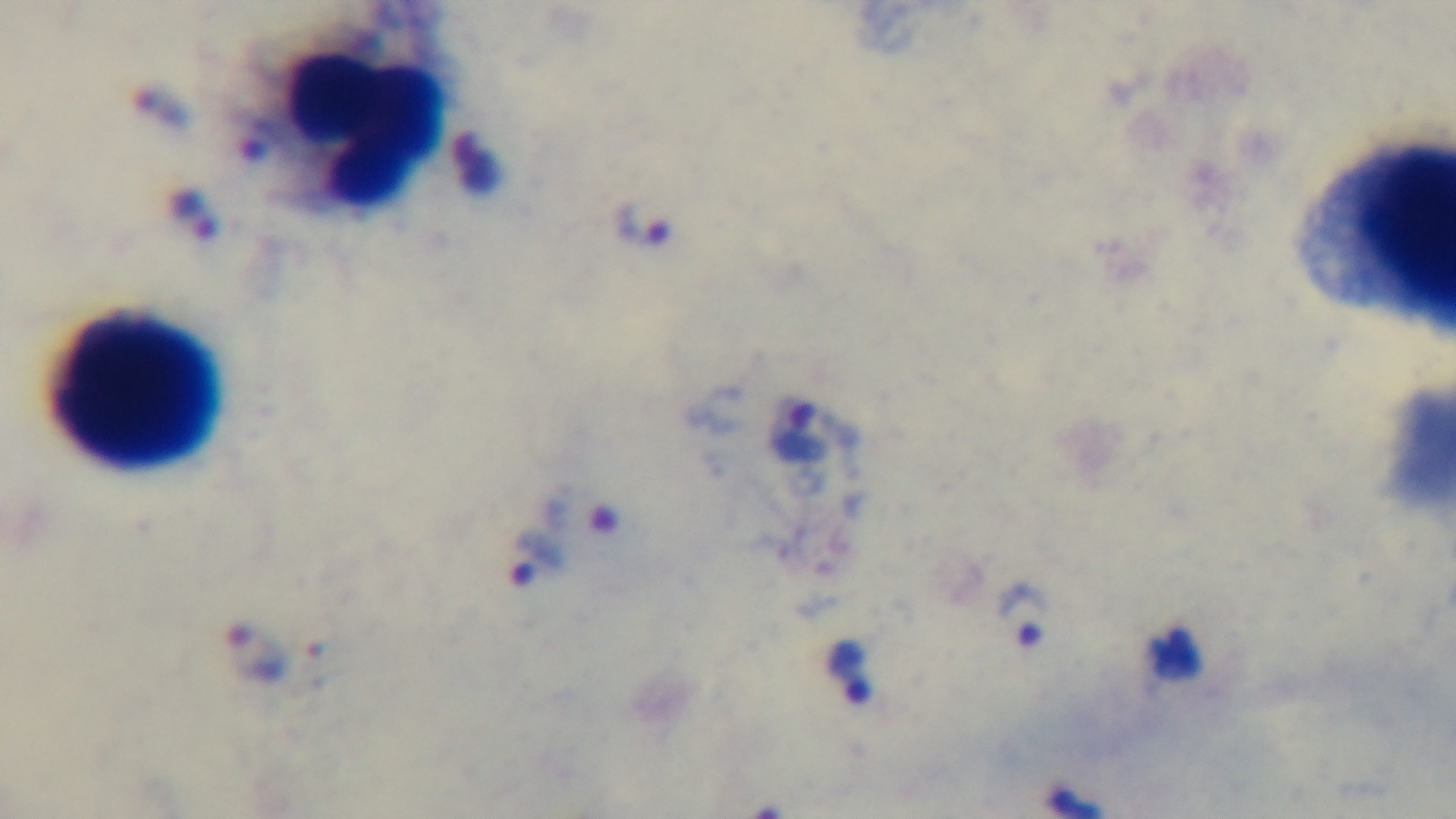 Light microscopy. Single field of view. 100x oil-immersion objective. Preparation: thick smear. Malaria status: positive. Captured with a mounted 4K digital camera. Giemsa-stained.